Give the position of every Plasmodium parasite visible.
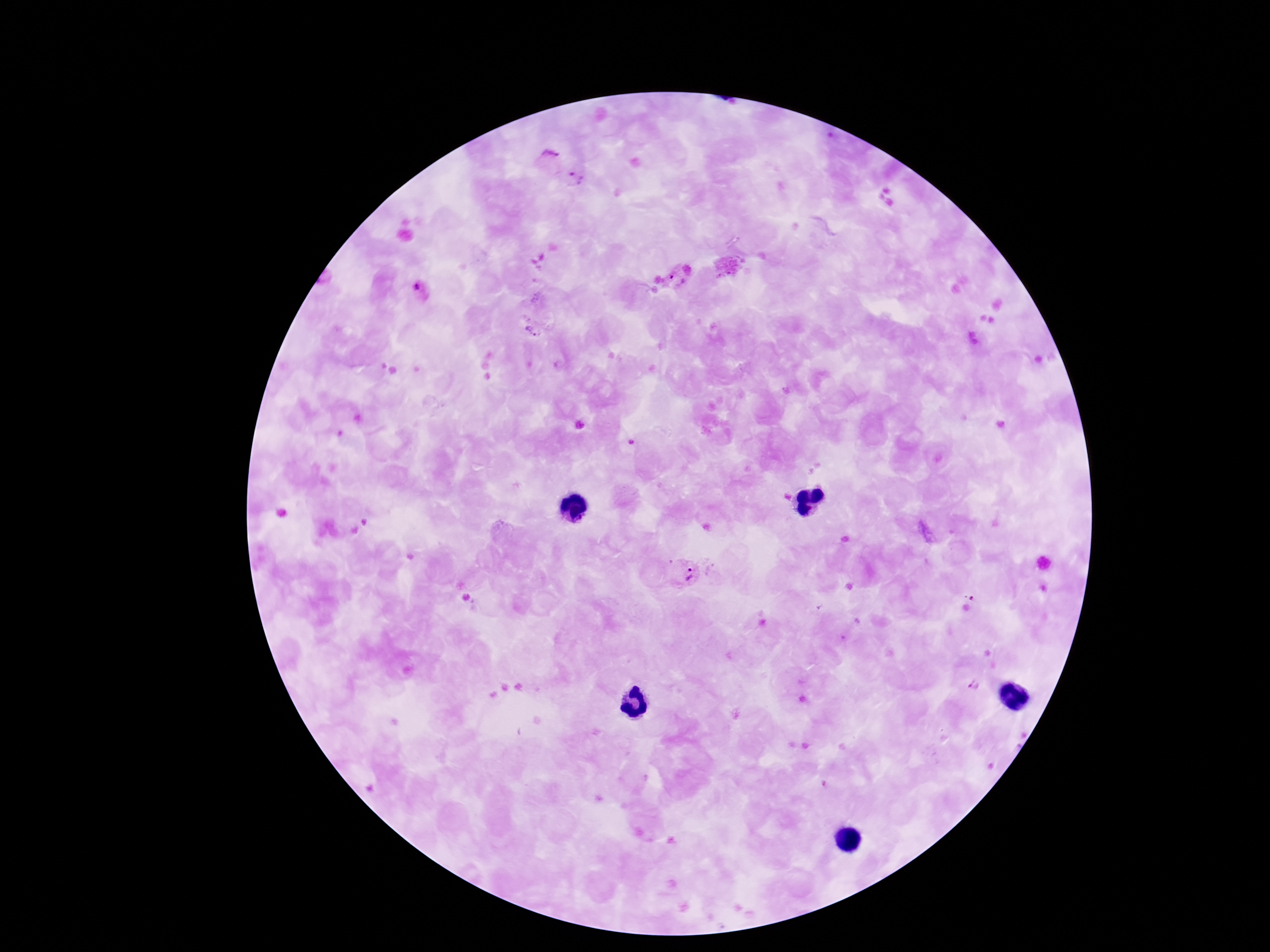

Approximate centers as [x, y] in pixels.
Plasmodium parasites: [550, 153], [580, 180], [677, 280], [422, 293], [532, 332], [691, 574], [975, 682].

Summary:
  - Magnification: 100x
  - Image size: 1270×952 pixels
  - Patient malaria status: infected
  - Field of view: single
  - Capture: smartphone camera through the microscope eyepiece
  - Preparation: thick blood film
  - Stain: Giemsa